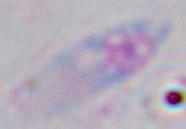

Toxoplasma gondii is shown. 1000x magnification. Micrograph.